State which cell type is depicted.
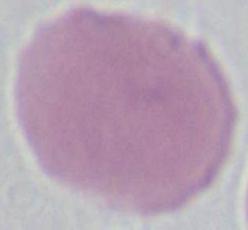
This is an erythrocyte.

{
  "modality": "photomicrograph",
  "magnification": "1000x"
}